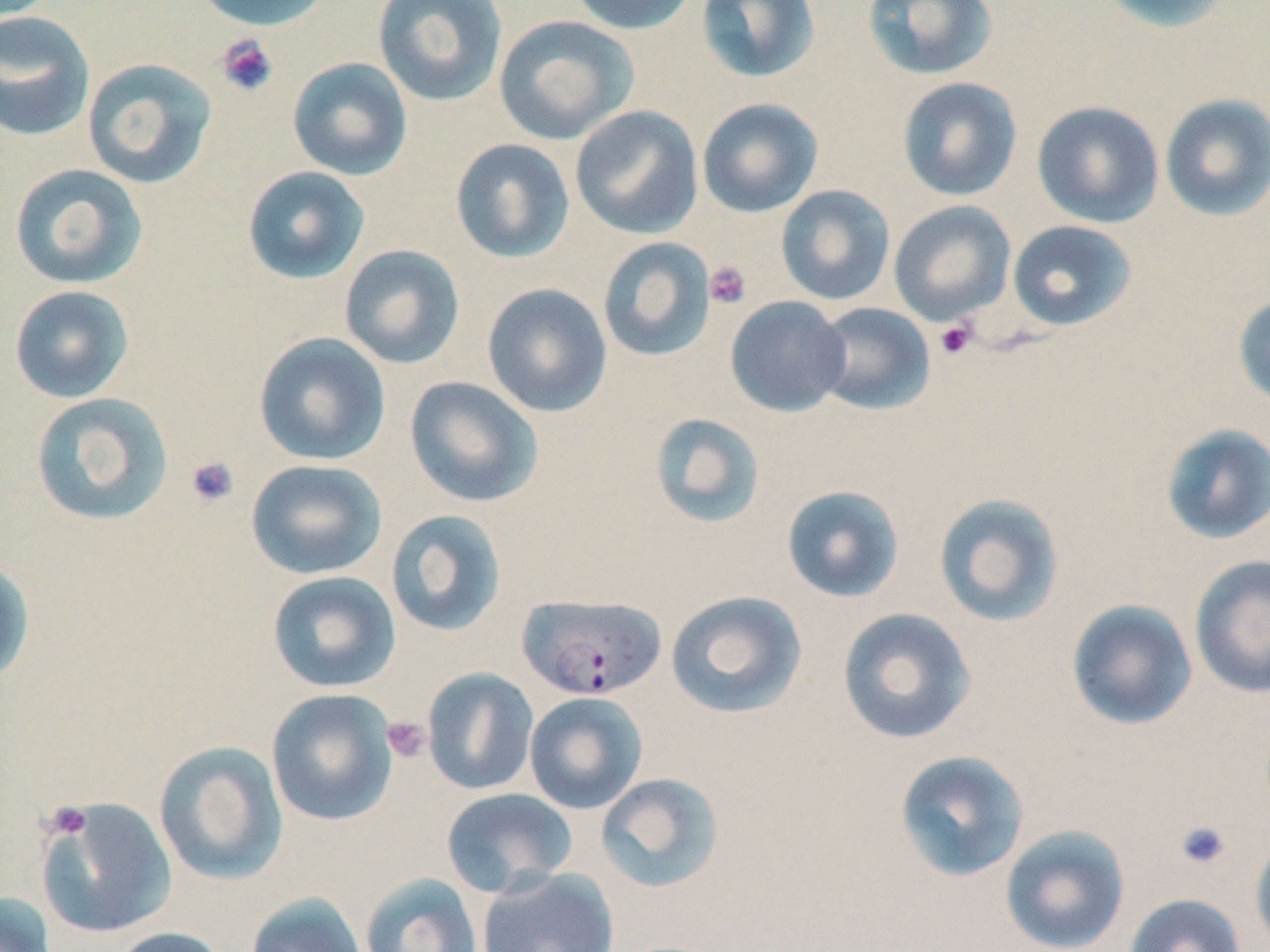
slide-level diagnosis = Plasmodium falciparum
field of view = one of a larger specimen
preparation = thin blood film
image size = 1270×952 pixels
uninfected red blood cell locations = approximate bounding boxes as named x1/y1/x2/y2 corners in pixels: (x1=192, y1=0, x2=333, y2=32), (x1=372, y1=0, x2=508, y2=107), (x1=566, y1=0, x2=698, y2=36), (x1=696, y1=0, x2=822, y2=84), (x1=861, y1=0, x2=999, y2=80), (x1=1096, y1=0, x2=1238, y2=33), (x1=0, y1=11, x2=96, y2=142), (x1=493, y1=15, x2=638, y2=145), (x1=287, y1=57, x2=413, y2=180), (x1=82, y1=58, x2=218, y2=189), (x1=897, y1=77, x2=1023, y2=202), (x1=1159, y1=93, x2=1270, y2=221), (x1=696, y1=97, x2=824, y2=217), (x1=1032, y1=100, x2=1164, y2=228), (x1=570, y1=105, x2=704, y2=239), (x1=450, y1=138, x2=575, y2=264), (x1=8, y1=163, x2=148, y2=290), (x1=242, y1=166, x2=371, y2=284), (x1=775, y1=184, x2=896, y2=306), (x1=888, y1=200, x2=1016, y2=325), (x1=1007, y1=220, x2=1138, y2=331), (x1=597, y1=237, x2=716, y2=362), (x1=338, y1=244, x2=465, y2=369), (x1=482, y1=283, x2=612, y2=418), (x1=9, y1=285, x2=134, y2=403), (x1=1232, y1=293, x2=1270, y2=409), (x1=725, y1=296, x2=851, y2=417), (x1=812, y1=302, x2=936, y2=415), (x1=253, y1=331, x2=391, y2=466), (x1=404, y1=376, x2=542, y2=507), (x1=30, y1=392, x2=174, y2=526), (x1=649, y1=412, x2=767, y2=528), (x1=1159, y1=424, x2=1270, y2=546), (x1=246, y1=459, x2=387, y2=580), (x1=781, y1=485, x2=905, y2=603), (x1=933, y1=492, x2=1065, y2=628), (x1=385, y1=509, x2=509, y2=637), (x1=0, y1=555, x2=34, y2=689), (x1=1189, y1=555, x2=1270, y2=698), (x1=267, y1=570, x2=401, y2=693), (x1=665, y1=590, x2=807, y2=719), (x1=1066, y1=599, x2=1198, y2=731), (x1=836, y1=607, x2=976, y2=745), (x1=422, y1=668, x2=539, y2=795), (x1=266, y1=688, x2=399, y2=826), (x1=524, y1=692, x2=648, y2=815), (x1=153, y1=740, x2=288, y2=885), (x1=893, y1=749, x2=1031, y2=883), (x1=595, y1=773, x2=726, y2=893), (x1=441, y1=787, x2=578, y2=897), (x1=35, y1=797, x2=179, y2=940), (x1=1000, y1=825, x2=1131, y2=952), (x1=1251, y1=837, x2=1270, y2=950), (x1=476, y1=867, x2=620, y2=952), (x1=359, y1=872, x2=483, y2=952), (x1=0, y1=891, x2=58, y2=952), (x1=245, y1=892, x2=368, y2=952), (x1=1123, y1=893, x2=1246, y2=952), (x1=108, y1=926, x2=232, y2=952)
stain = May-Grünwald-Giemsa
platelet locations = approximate bounding boxes as named x1/y1/x2/y2 corners in pixels: (x1=215, y1=34, x2=279, y2=97), (x1=704, y1=261, x2=751, y2=308), (x1=935, y1=320, x2=977, y2=359), (x1=185, y1=456, x2=240, y2=509), (x1=381, y1=715, x2=431, y2=763), (x1=42, y1=801, x2=93, y2=841), (x1=1174, y1=819, x2=1232, y2=870)
magnification = 1000x
Plasmodium falciparum-infected red blood cell locations = approximate bounding boxes as named x1/y1/x2/y2 corners in pixels: (x1=517, y1=594, x2=668, y2=701)
modality = optical microscopy